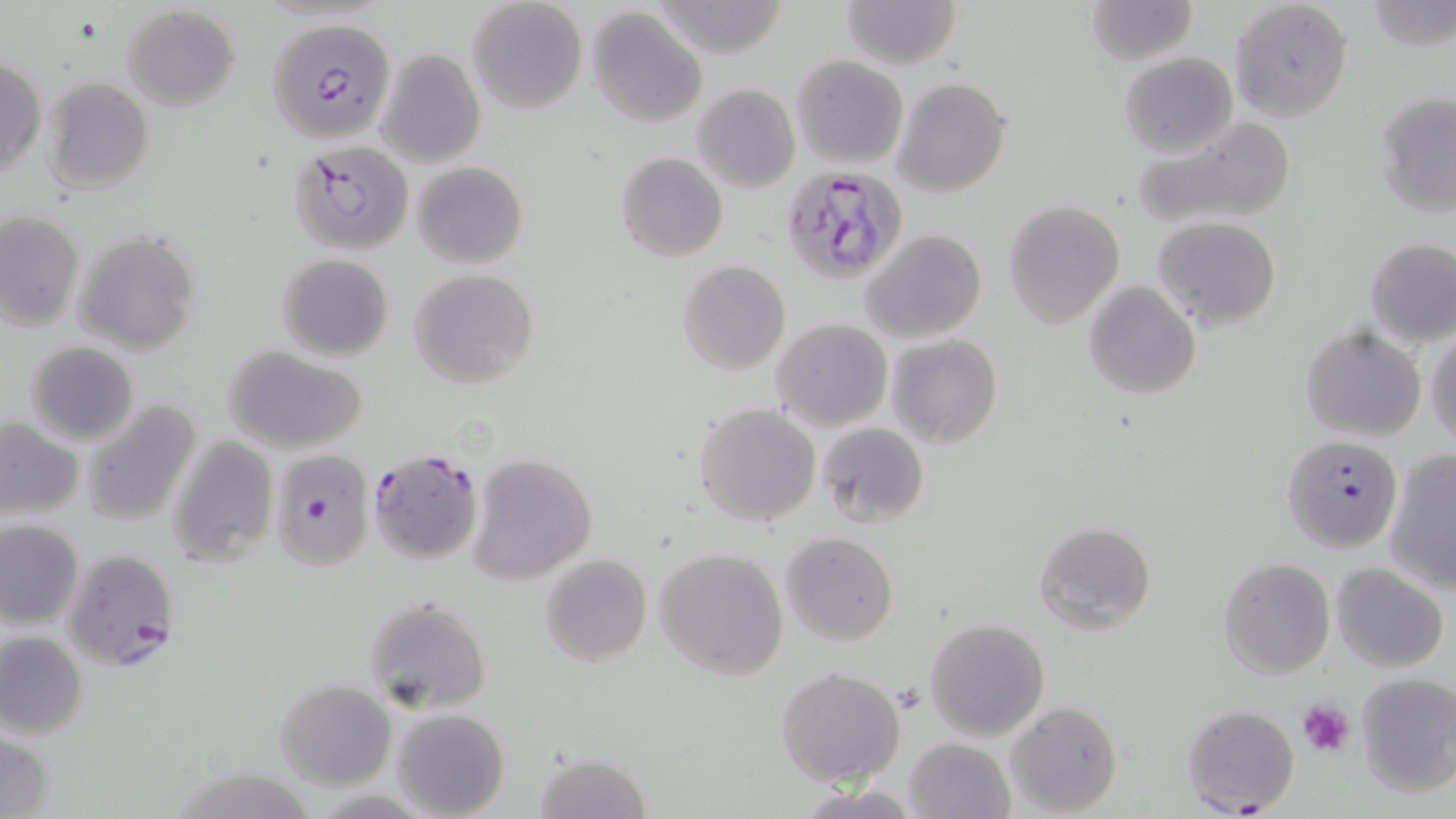
slide_level_diagnosis: Plasmodium falciparum
modality: light microscopy
uninfected_red_blood_cell_locations: 'approximate bounding boxes as [x1, y1, x2, y2] in pixels: [466, 0, 589, 116], [841, 0, 959, 70], [1081, 0, 1199, 65], [1228, 0, 1353, 123], [1365, 0, 1455, 51], [650, 1, 788, 58], [122, 5, 241, 111], [585, 8, 708, 127], [375, 49, 486, 168], [1117, 51, 1238, 157], [792, 55, 908, 169], [1, 57, 46, 177], [42, 76, 154, 195], [893, 76, 1012, 200], [692, 84, 800, 193], [1374, 91, 1456, 217], [1129, 117, 1300, 232], [616, 152, 728, 263], [413, 161, 527, 269], [1003, 200, 1124, 328], [0, 211, 85, 330], [1153, 217, 1281, 331], [859, 229, 987, 346], [73, 231, 201, 355], [1364, 237, 1456, 349], [277, 254, 394, 362], [677, 261, 790, 375], [406, 273, 535, 393], [1083, 282, 1201, 400], [771, 319, 893, 433], [1424, 324, 1456, 448], [1300, 325, 1426, 442], [885, 334, 1003, 450], [24, 341, 140, 446], [221, 344, 371, 455], [79, 400, 203, 527], [694, 402, 822, 528], [0, 418, 83, 519], [817, 423, 929, 529], [168, 436, 279, 568], [1382, 447, 1456, 594], [467, 453, 597, 585], [0, 520, 85, 628], [1033, 520, 1157, 635], [780, 530, 899, 646], [653, 547, 789, 680], [539, 554, 652, 666], [1217, 556, 1335, 680], [1331, 562, 1450, 673], [361, 595, 491, 716], [925, 617, 1051, 742], [0, 632, 88, 738], [776, 666, 906, 787], [1354, 672, 1456, 797], [275, 679, 397, 788], [1004, 700, 1123, 817], [391, 708, 509, 819], [1, 731, 54, 818], [903, 737, 1016, 819], [534, 750, 654, 819], [167, 765, 318, 819]'
image_size: 1456×819 pixels
stain: May-Grünwald-Giemsa
field_of_view: single
preparation: thin blood film
plasmodium_falciparum_infected_red_blood_cell_locations: 'approximate bounding boxes as [x1, y1, x2, y2] in pixels: [269, 17, 397, 143], [290, 141, 413, 254], [781, 165, 908, 282], [1283, 433, 1403, 555], [367, 448, 484, 564], [269, 449, 375, 573], [61, 547, 181, 673], [1180, 704, 1300, 814]'
platelet_locations: 'approximate bounding boxes as [x1, y1, x2, y2] in pixels: [1297, 699, 1354, 758]'
magnification: 1000x